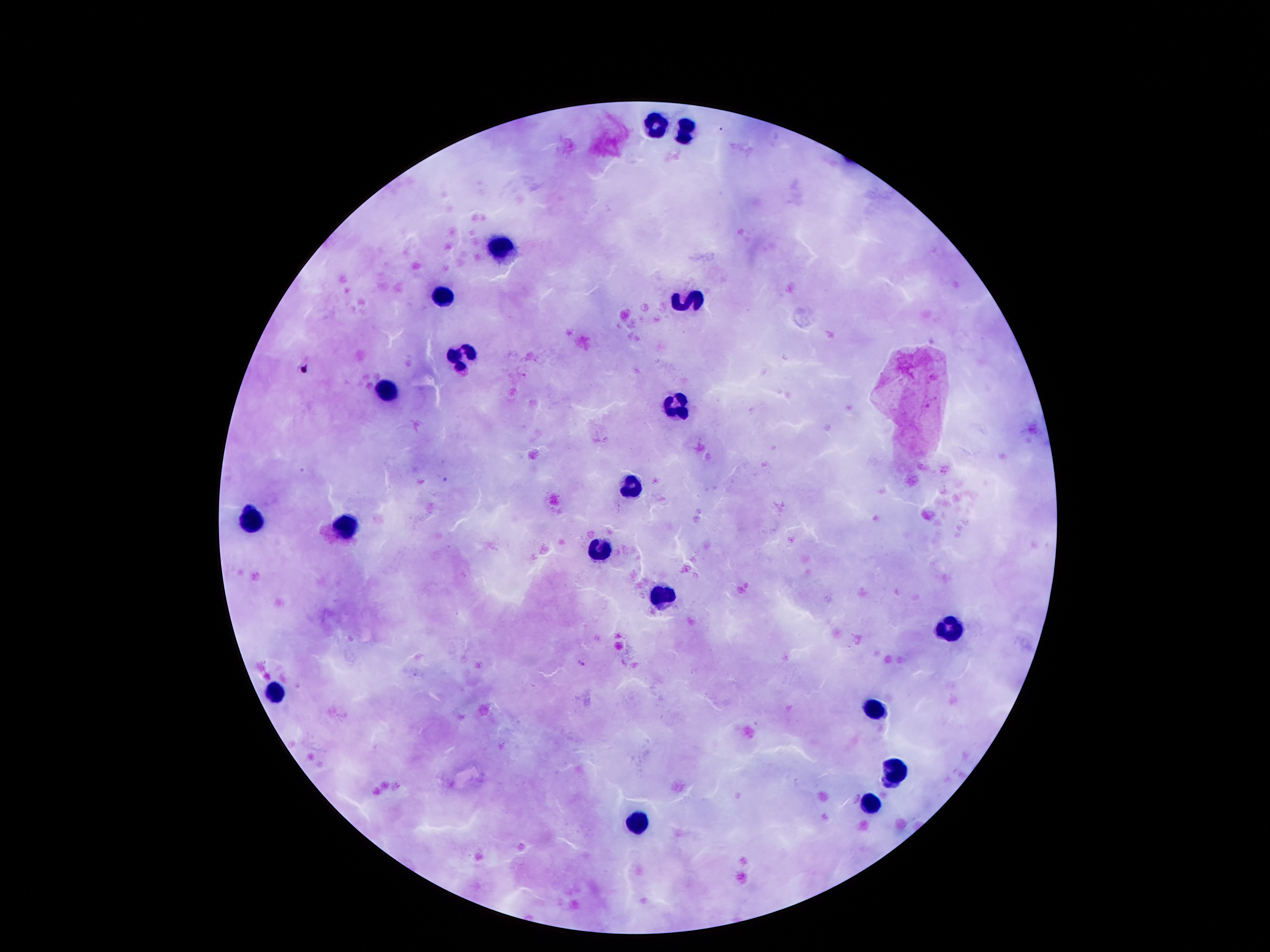 Approximate object centers, in pixels from the top-left corner. Leukocyte locations: (x=661, y=123), (x=687, y=131), (x=498, y=249), (x=447, y=295), (x=689, y=305), (x=462, y=356), (x=391, y=388), (x=678, y=410), (x=630, y=486), (x=252, y=520), (x=348, y=526), (x=603, y=551), (x=664, y=597), (x=955, y=631), (x=279, y=690), (x=876, y=709), (x=894, y=774), (x=871, y=807), (x=642, y=822). Plasmodium parasite locations: (x=447, y=479), (x=581, y=662). Thick blood film. Image is 1270×952 pixels. One field from this slide. 100x magnification. Photographed through the microscope eyepiece with a smartphone camera. Giemsa stain. Patient malaria status: infected with Plasmodium falciparum.